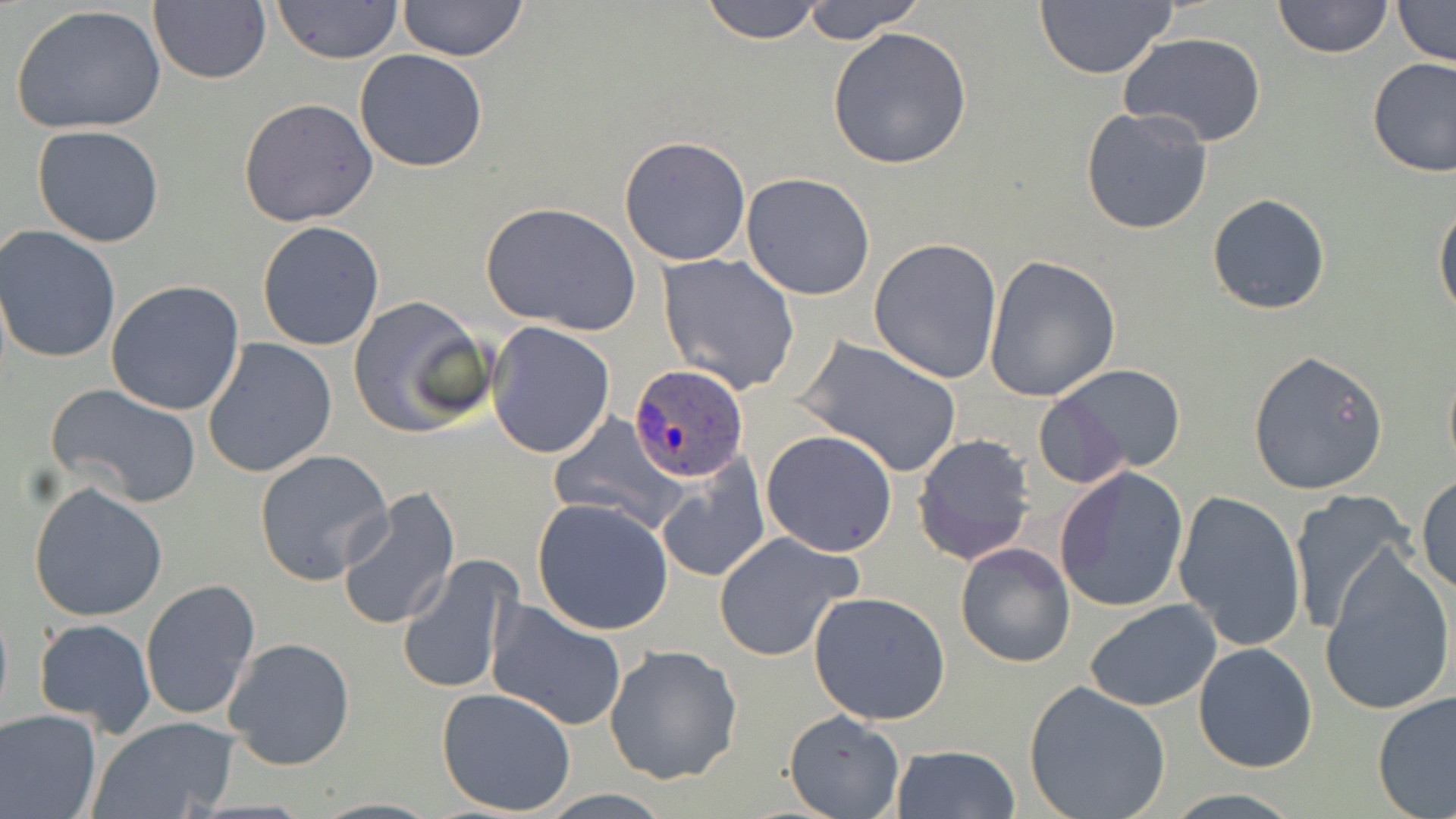

Summary:
  - Coordinate format: approximate bounding boxes as (x1,y1)-(x2,y2) corner pairs in pixels
  - Uninfected red blood cell locations: (149,0)-(271,85), (396,0)-(530,63), (699,0)-(827,45), (798,0)-(927,43), (1272,0)-(1393,59), (1392,0)-(1456,67), (271,1)-(404,64), (1034,2)-(1178,79), (8,4)-(167,136), (826,26)-(972,168), (1119,33)-(1267,148), (355,48)-(489,172), (1366,57)-(1456,177), (238,98)-(378,227), (1081,107)-(1214,235), (31,124)-(166,247), (618,135)-(752,267), (741,173)-(876,301), (1206,193)-(1331,316), (480,200)-(641,336), (1433,200)-(1455,325), (257,221)-(386,351), (0,226)-(122,364), (869,237)-(1003,383), (657,252)-(801,393), (983,255)-(1120,402), (105,280)-(245,416), (347,295)-(493,440), (486,323)-(616,458), (796,335)-(963,479), (202,338)-(337,478), (1246,349)-(1389,496), (1441,357)-(1456,480), (1042,363)-(1188,479), (46,382)-(202,509), (1031,395)-(1130,489), (548,414)-(685,534), (762,430)-(897,556), (913,433)-(1035,564), (253,448)-(392,586), (655,458)-(771,581), (1053,465)-(1190,614), (1416,474)-(1455,593), (29,481)-(169,623), (334,488)-(460,633), (1173,489)-(1307,651), (1287,491)-(1416,636), (532,499)-(673,636), (713,530)-(864,662), (954,541)-(1075,668), (1320,545)-(1455,718), (398,556)-(520,696), (140,578)-(259,721), (807,590)-(953,726), (485,599)-(627,731), (1084,600)-(1222,712), (31,618)-(157,738), (222,636)-(355,771), (1193,641)-(1319,773), (604,645)-(742,785), (1023,681)-(1172,819), (436,687)-(578,816), (1372,691)-(1456,819), (0,707)-(102,819), (783,708)-(906,818), (89,718)-(240,818), (889,743)-(1021,819), (308,796)-(445,818)
  - Plasmodium ovale-infected red blood cell locations: (628,363)-(749,482)
  - Slide-level diagnosis: Plasmodium ovale
  - Modality: light microscopy
  - Stain: May-Grünwald-Giemsa
  - Magnification: 1000x
  - Preparation: thin blood smear
  - Field of view: single
  - Image size: 1456×819 pixels